Name the parasite shown.
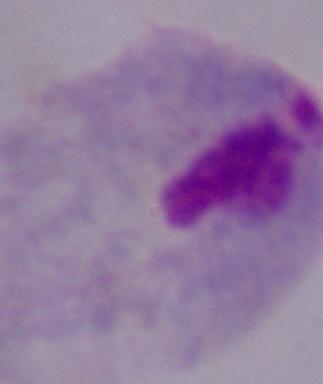

A trichomonad.

magnification = 1000x
modality = photomicrograph